Outline each blood parasite and name the species.
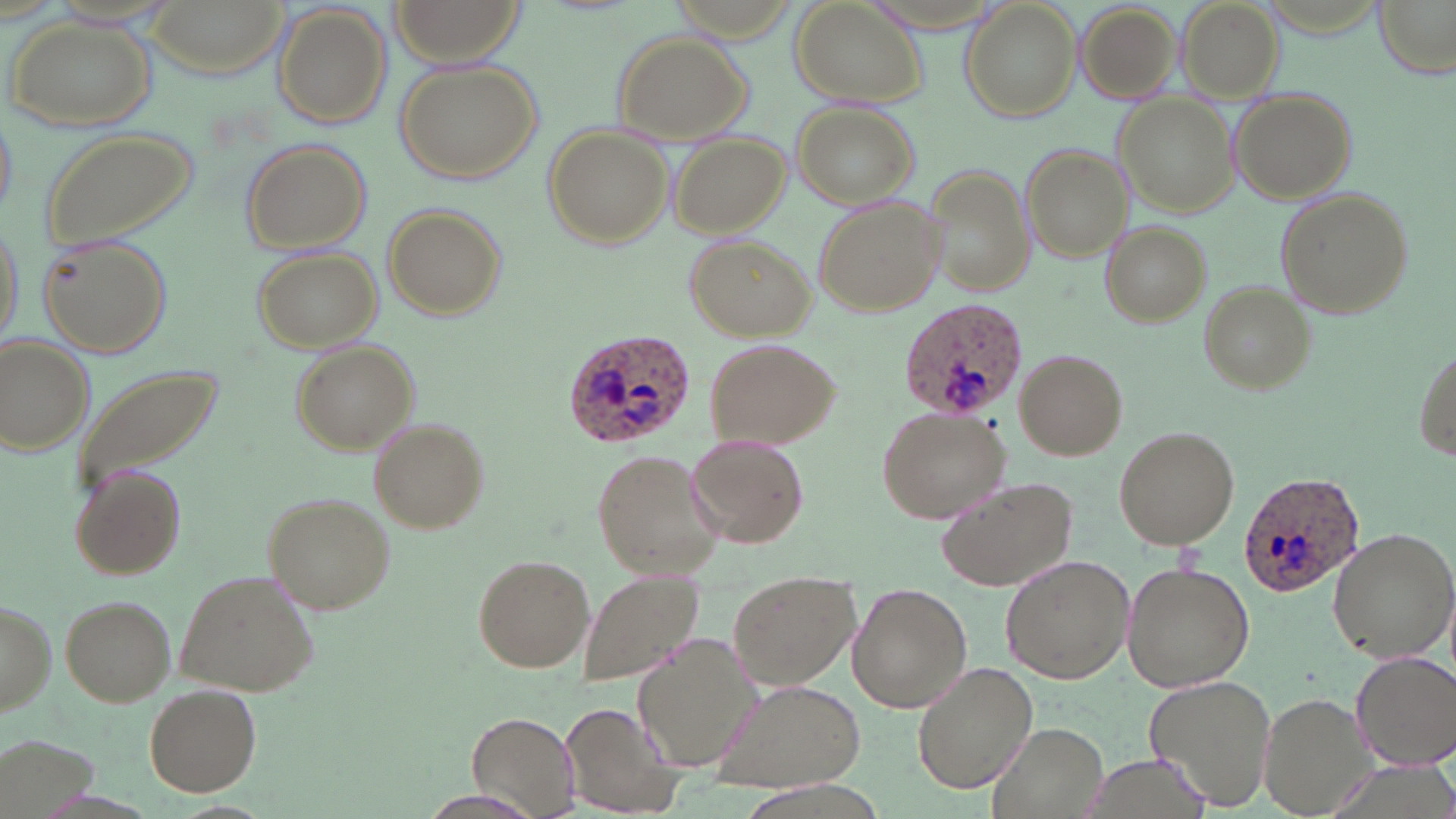

Approximate bounding boxes as (x1, y1, x2, y2) in pixels.
Plasmodium ovale-infected red blood cells: (897, 295, 1026, 421), (558, 329, 697, 448), (1238, 469, 1366, 595).
No Plasmodium falciparum, Plasmodium malariae, Plasmodium vivax, Babesia divergens, or Trypanosoma brucei observed.

slide-level diagnosis = Plasmodium ovale
modality = optical microscopy
image size = 1456×819 pixels
preparation = thin blood smear
uninfected red blood cell locations = approximate bounding boxes as (x1, y1, x2, y2) in pixels: (143, 0, 288, 77), (388, 0, 527, 63), (1176, 0, 1283, 99), (1375, 0, 1454, 76), (789, 1, 926, 107), (959, 1, 1082, 122), (1075, 1, 1183, 103), (273, 4, 390, 128), (5, 14, 156, 130), (612, 29, 752, 143), (393, 58, 543, 185), (1231, 90, 1357, 202), (1115, 94, 1242, 217), (0, 104, 17, 227), (793, 104, 916, 208), (545, 125, 672, 246), (37, 126, 201, 251), (670, 131, 790, 237), (240, 138, 371, 254), (1020, 144, 1134, 262), (921, 166, 1034, 297), (1273, 186, 1413, 320), (814, 198, 947, 315), (384, 204, 509, 320), (0, 214, 25, 348), (1101, 220, 1211, 326), (35, 232, 173, 358), (684, 235, 814, 338), (252, 246, 383, 352), (1198, 281, 1316, 395), (0, 336, 96, 454), (701, 336, 839, 451), (292, 342, 416, 453), (1414, 345, 1455, 458), (1014, 348, 1127, 461), (68, 363, 226, 497), (875, 405, 1013, 524), (371, 421, 489, 532), (1112, 425, 1240, 549), (687, 435, 810, 548), (592, 449, 725, 580), (71, 464, 188, 582), (936, 476, 1079, 590), (263, 494, 397, 616), (1328, 528, 1456, 665), (473, 554, 594, 672), (999, 555, 1134, 684), (1122, 560, 1255, 693), (178, 568, 320, 696), (580, 568, 706, 687), (728, 570, 860, 690), (848, 584, 972, 712), (63, 596, 175, 706), (2, 598, 56, 715), (635, 637, 765, 770), (1351, 652, 1456, 770), (913, 662, 1036, 794), (1146, 673, 1279, 811), (714, 680, 867, 793), (143, 685, 261, 797), (1259, 691, 1379, 817), (558, 703, 682, 819), (466, 710, 582, 815), (989, 722, 1108, 819), (421, 790, 539, 817)
stain = May-Grünwald-Giemsa
field of view = one of a larger specimen
magnification = 1000x